Report the malaria status of this cell.
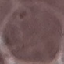

It is uninfected.

stain = Giemsa
capture = smartphone camera at the microscope eyepiece
preparation = thin blood smear
image type = cell patch, automatically extracted from a larger field of view and resized to 64 × 64 pixels